Locate every blood parasite and identify its species.
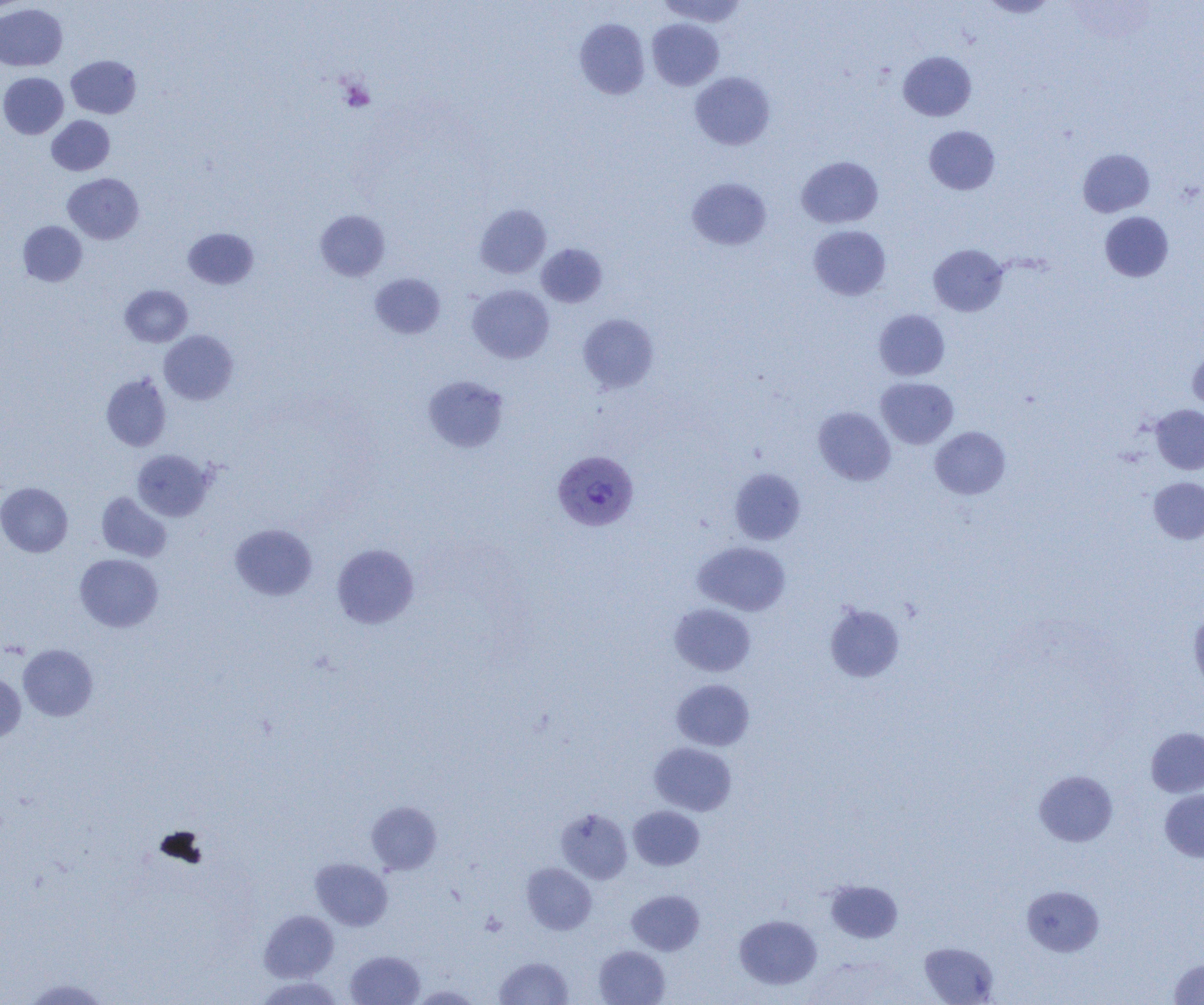

Approximate bounding boxes as [x1, y1, x2, y2] in pixels.
Plasmodium vivax-infected red blood cells: [553, 450, 639, 531].
No Plasmodium falciparum, Plasmodium ovale, Plasmodium malariae, Babesia divergens, or Trypanosoma brucei observed.

slide_level_diagnosis: Plasmodium vivax
image_size: 1204×1005 pixels
preparation: thin blood film
modality: light microscopy
uninfected_red_blood_cell_locations: 'approximate bounding boxes as [x1, y1, x2, y2] in pixels: [657, 0, 749, 27], [980, 0, 1058, 18], [0, 3, 67, 71], [574, 18, 650, 99], [647, 18, 724, 90], [898, 51, 976, 121], [66, 55, 141, 119], [0, 72, 68, 138], [690, 72, 775, 150], [47, 115, 114, 175], [924, 126, 1000, 195], [1078, 148, 1155, 217], [797, 156, 883, 228], [63, 173, 144, 244], [686, 177, 771, 250], [475, 204, 551, 278], [315, 210, 390, 281], [1100, 212, 1173, 281], [18, 221, 87, 286], [808, 225, 891, 300], [183, 228, 259, 289], [536, 243, 607, 307], [928, 244, 1008, 316], [370, 274, 445, 339], [467, 284, 555, 363], [120, 285, 192, 347], [874, 309, 950, 380], [578, 314, 659, 393], [159, 330, 238, 405], [1187, 347, 1204, 413], [101, 373, 171, 451], [422, 375, 510, 452], [876, 377, 958, 448], [1151, 405, 1204, 474], [813, 406, 895, 485], [930, 426, 1011, 499], [132, 450, 215, 520], [729, 468, 805, 545], [1148, 477, 1204, 544], [0, 482, 73, 557], [97, 492, 172, 562], [230, 523, 317, 600], [693, 541, 791, 616], [332, 543, 419, 628], [75, 554, 163, 632], [670, 603, 756, 676], [825, 603, 905, 682], [1189, 609, 1204, 692], [18, 644, 98, 721], [0, 672, 25, 743], [671, 679, 755, 750], [1146, 727, 1204, 797], [649, 742, 736, 816], [1034, 770, 1118, 846], [1160, 789, 1204, 862], [366, 801, 442, 874], [628, 806, 704, 871], [555, 807, 633, 884], [310, 858, 393, 931], [521, 863, 596, 934], [826, 880, 903, 943], [1021, 885, 1104, 956], [627, 890, 704, 955], [259, 910, 338, 982], [734, 914, 822, 990], [919, 941, 999, 1004], [594, 945, 670, 1005], [345, 950, 425, 1005], [494, 956, 573, 1005], [1169, 957, 1204, 1004], [255, 976, 345, 1004], [22, 978, 111, 1004], [410, 984, 483, 1004]'
field_of_view: one of a larger specimen
platelet_locations: 'approximate bounding boxes as [x1, y1, x2, y2] in pixels: [338, 78, 375, 112]'
magnification: 1000x